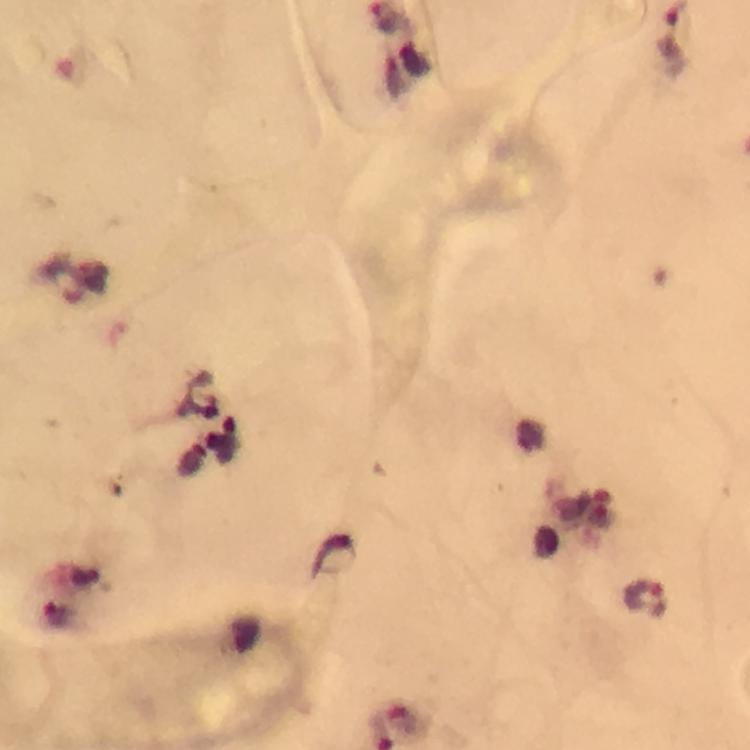
preparation = thick blood film
immersion oil = used
Plasmodium parasite locations = approximate centers as (x, y) in pixels: (86, 285), (334, 555), (646, 598), (56, 615)
capture = smartphone camera through the microscope
cropped from = one field of view
image size = 750×750 pixels
context = from a malaria diagnostic workup
magnification = 100x
stain = Giemsa